Identify the blood parasite species.
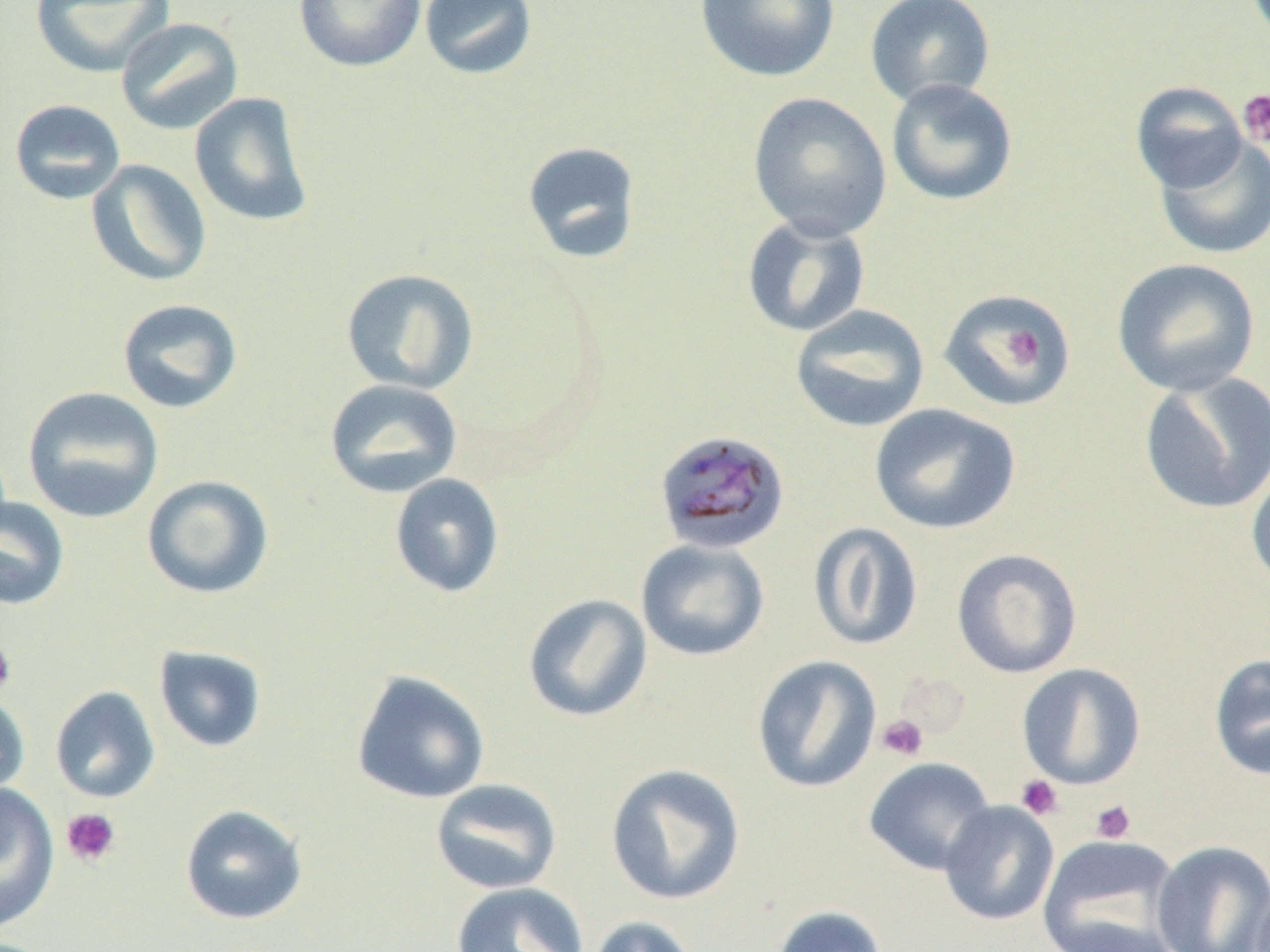
Plasmodium malariae.

magnification = 1000x
Plasmodium malariae-infected red blood cell locations = approximate bounding boxes as (x1,y1)-(x2,y2) corner pairs in pixels: (652,429)-(791,555)
modality = optical microscopy
platelet locations = approximate bounding boxes as (x1,y1)-(x2,y2) corner pairs in pixels: (1237,89)-(1270,150), (1005,325)-(1044,371), (0,637)-(17,696), (876,714)-(929,761), (1015,774)-(1064,821), (1089,799)-(1136,843), (61,808)-(122,867)
field of view = single
preparation = thin blood smear
uninfected red blood cell locations = approximate bounding boxes as (x1,y1)-(x2,y2) corner pairs in pixels: (31,0)-(174,77), (294,0)-(427,72), (419,0)-(539,81), (694,0)-(840,82), (864,0)-(996,109), (115,17)-(244,135), (885,77)-(1019,207), (1129,81)-(1248,193), (747,91)-(892,241), (189,92)-(315,228), (9,99)-(126,205), (1152,134)-(1270,260), (522,141)-(642,265), (86,159)-(212,287), (741,214)-(871,338), (1111,258)-(1261,396), (341,268)-(479,395), (938,288)-(1077,411), (116,298)-(244,413), (789,303)-(930,433), (1138,371)-(1270,516), (324,378)-(463,499), (22,386)-(164,524), (869,403)-(1021,535), (1247,458)-(1270,594), (389,473)-(505,598), (141,474)-(275,600), (0,495)-(70,610), (807,523)-(924,651), (635,538)-(770,661), (951,548)-(1083,678), (522,592)-(653,723), (153,644)-(269,753), (1208,653)-(1270,781), (751,655)-(882,794), (1017,663)-(1146,790), (350,669)-(490,805), (46,683)-(158,799), (0,688)-(31,802), (863,757)-(997,876), (605,763)-(746,905), (430,778)-(562,895), (0,782)-(60,934), (939,801)-(1059,926), (179,804)-(309,925), (1036,833)-(1183,952), (1150,840)-(1270,952), (449,881)-(590,952), (1251,886)-(1270,952), (769,905)-(889,952), (584,915)-(703,952)
image size = 1270×952 pixels